Identify the blood parasite species.
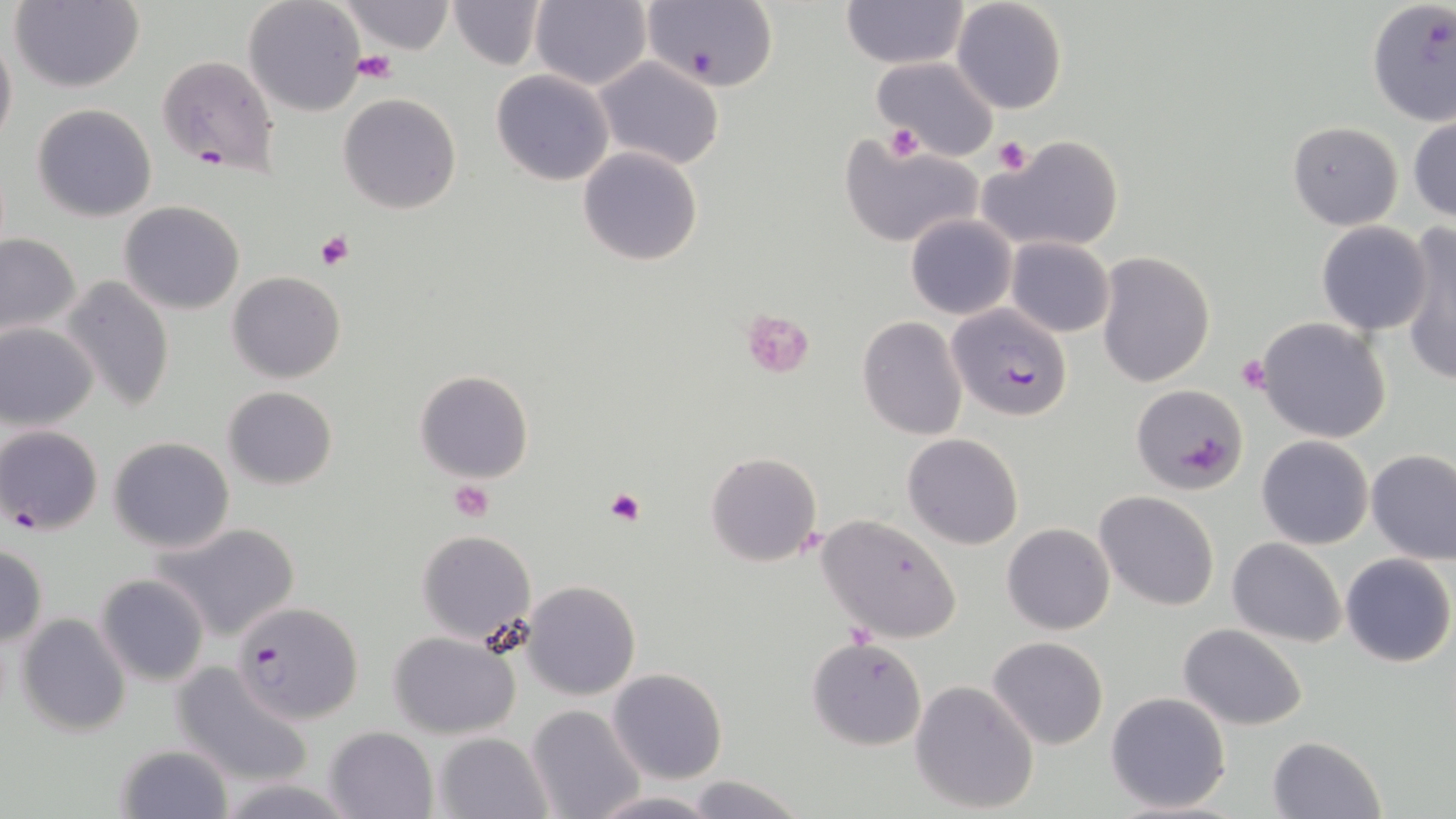

Plasmodium falciparum.

Approximate bounding boxes as (x1, y1, x2, y2) in pixels. Plasmodium falciparum-infected red blood cell locations: (946, 304, 1073, 420), (0, 424, 103, 536), (231, 600, 365, 724). Platelet locations: (353, 50, 398, 85), (885, 125, 924, 159), (995, 135, 1032, 174), (197, 149, 226, 170), (313, 229, 355, 272), (740, 310, 817, 379), (1237, 352, 1272, 393), (447, 479, 495, 524), (605, 487, 645, 527). Uninfected red blood cell locations: (9, 0, 146, 93), (242, 0, 367, 118), (340, 0, 457, 56), (531, 0, 653, 90), (642, 0, 779, 91), (839, 0, 969, 71), (951, 0, 1068, 115), (450, 1, 543, 70), (1365, 1, 1456, 126), (0, 28, 16, 153), (585, 51, 717, 163), (157, 54, 280, 175), (872, 56, 999, 161), (490, 70, 615, 186), (337, 92, 463, 215), (32, 104, 158, 222), (1408, 111, 1456, 224), (1286, 121, 1402, 231), (839, 133, 982, 248), (982, 137, 1125, 255), (577, 147, 704, 266), (118, 202, 246, 315), (906, 215, 1016, 318), (1316, 221, 1434, 335), (1395, 223, 1456, 387), (0, 231, 83, 337), (1006, 236, 1116, 337), (1097, 251, 1216, 387), (228, 271, 345, 384), (62, 276, 175, 413), (859, 316, 968, 440), (1256, 316, 1392, 444), (0, 323, 99, 429), (414, 370, 533, 483), (1131, 383, 1250, 495), (223, 386, 338, 490), (902, 432, 1023, 549), (1256, 435, 1374, 550), (108, 436, 234, 554), (1366, 448, 1456, 564), (705, 451, 822, 568), (1095, 490, 1219, 610), (816, 514, 964, 643), (153, 521, 302, 642), (1002, 523, 1115, 635), (417, 530, 536, 645), (1226, 537, 1346, 645), (0, 545, 49, 649), (1339, 553, 1454, 667), (96, 574, 211, 687), (522, 579, 640, 701), (17, 613, 129, 736), (1178, 623, 1310, 731), (389, 631, 521, 740), (806, 635, 927, 751), (988, 636, 1110, 751), (172, 662, 314, 787), (609, 668, 728, 784), (908, 680, 1040, 814), (1104, 690, 1233, 815), (527, 704, 646, 819), (325, 726, 437, 818), (434, 731, 550, 818), (1267, 736, 1386, 819), (115, 743, 231, 818), (684, 774, 810, 818), (216, 776, 356, 818), (588, 791, 719, 819). 1000x magnification. Optical microscopy. May-Grünwald-Giemsa-stained preparation. Image is 1456×819 pixels. One field of a larger specimen. Thin blood film.